Name the parasite shown.
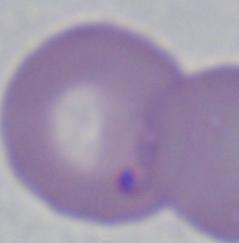

Babesia.

1000x magnification. Photomicrograph.